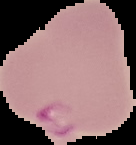

malaria status = parasitized
image size = 136×145 pixels
preparation = thin blood smear
image type = segmented cell region on a black background